Give the position of every Plasmodium parasite.
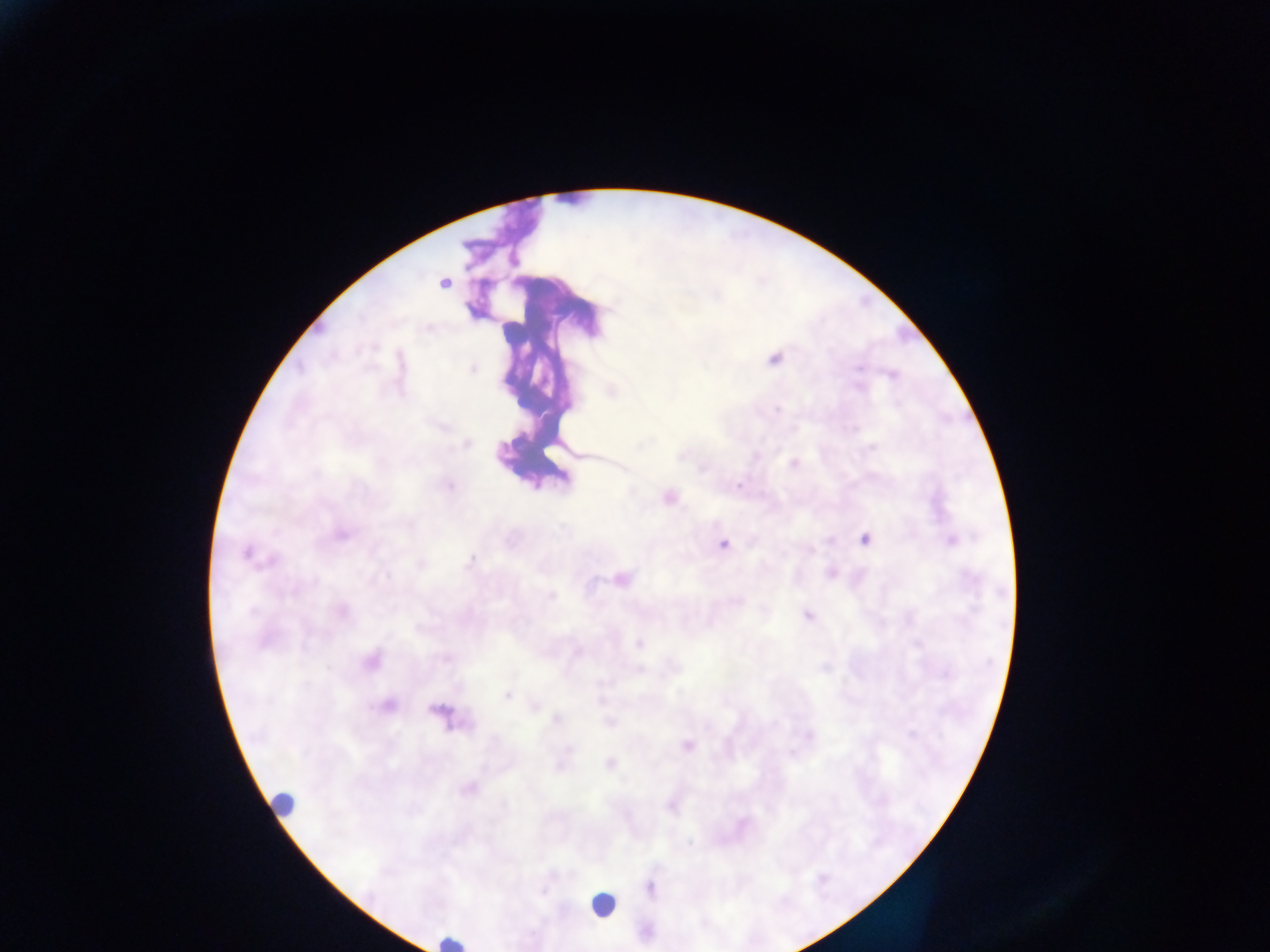
Approximate centers as (x, y) in pixels.
Plasmodium parasites: (443, 282), (774, 358), (472, 369), (892, 375), (610, 391), (465, 443), (793, 464), (667, 497), (340, 533), (865, 539), (950, 540), (722, 544), (246, 552), (830, 572), (619, 579), (340, 611), (806, 614), (639, 643), (371, 659), (507, 694), (387, 705), (534, 707), (440, 712), (687, 746), (610, 763), (468, 787), (649, 887).

preparation = thick blood film
capture = mobile-phone photograph through a microscope
field of view = single
leukocyte locations = approximate centers as (x, y) in pixels: (284, 804), (601, 905), (449, 941)
image size = 1270×952 pixels
country = Ghana